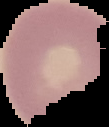

malaria_status: uninfected
image_size: 109×127 pixels
preparation: thin blood smear
image_type: cell region segmented out of the field of view; surrounding area masked to black